Assess this cell for malaria.
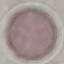

Uninfected.

Automatically extracted cell patch, resized to 64 × 64 pixels. Thin smear of blood. Acquired by smartphone through the microscope eyepiece. Giemsa-stained preparation.